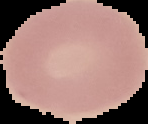
Summary:
  - Image type: segmented cell region on a black background
  - Result: no malaria parasites detected
  - Image size: 148×124 pixels
  - Preparation: thin blood film